Classify this cell by malaria status.
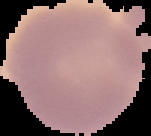
Uninfected.

The area outside the segmented cell region is set to black. From a thin blood film. Image is 151×136 pixels.